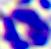

Captured at 400x magnification. A white blood cell is seen. Micrograph.